State the preparation type.
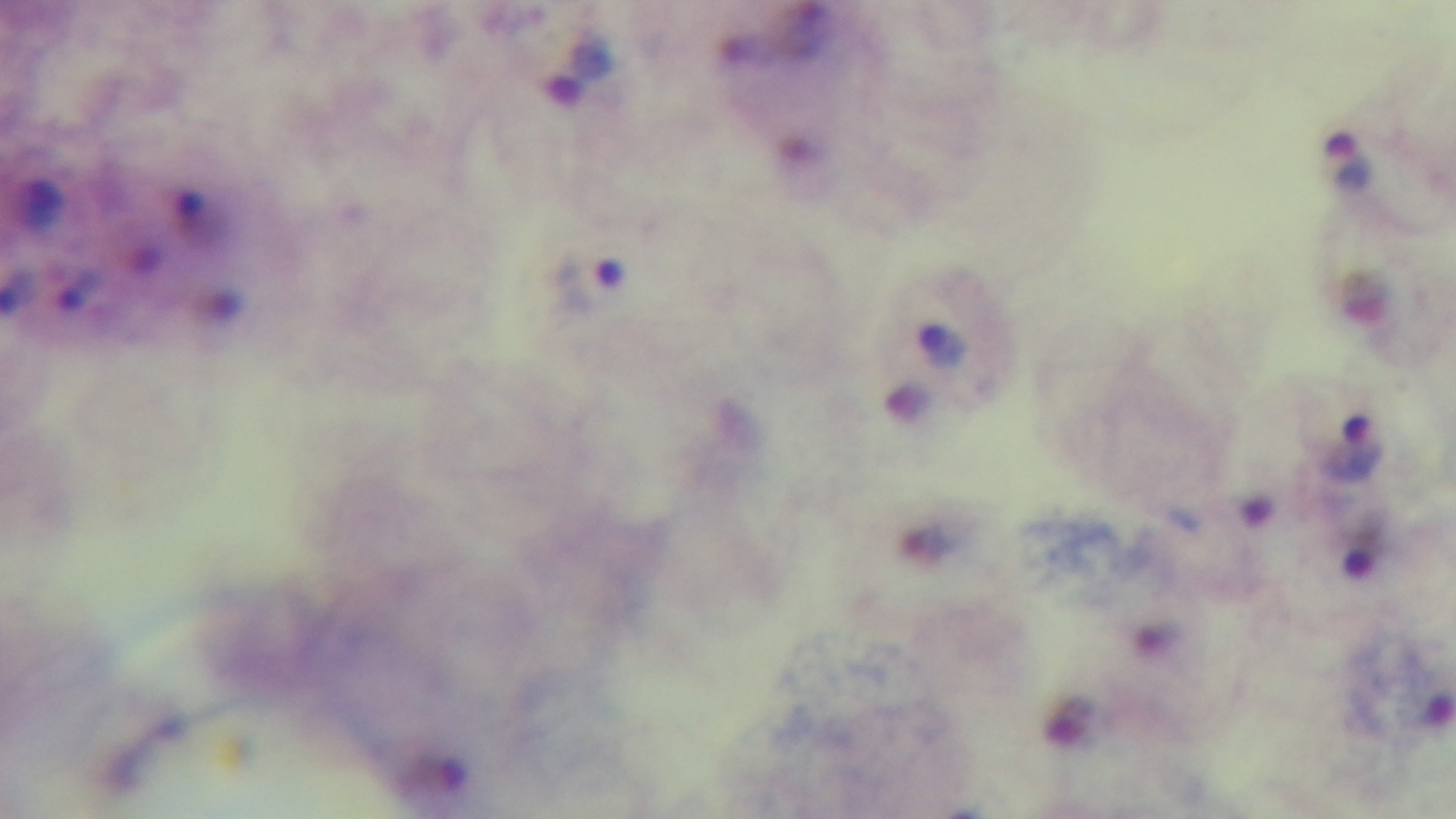

Thick.

capture = mounted 4K digital camera
field of view = single
malaria status = positive
stain = Giemsa
modality = light microscopy
objective = 100x oil immersion